Name the blood parasite species.
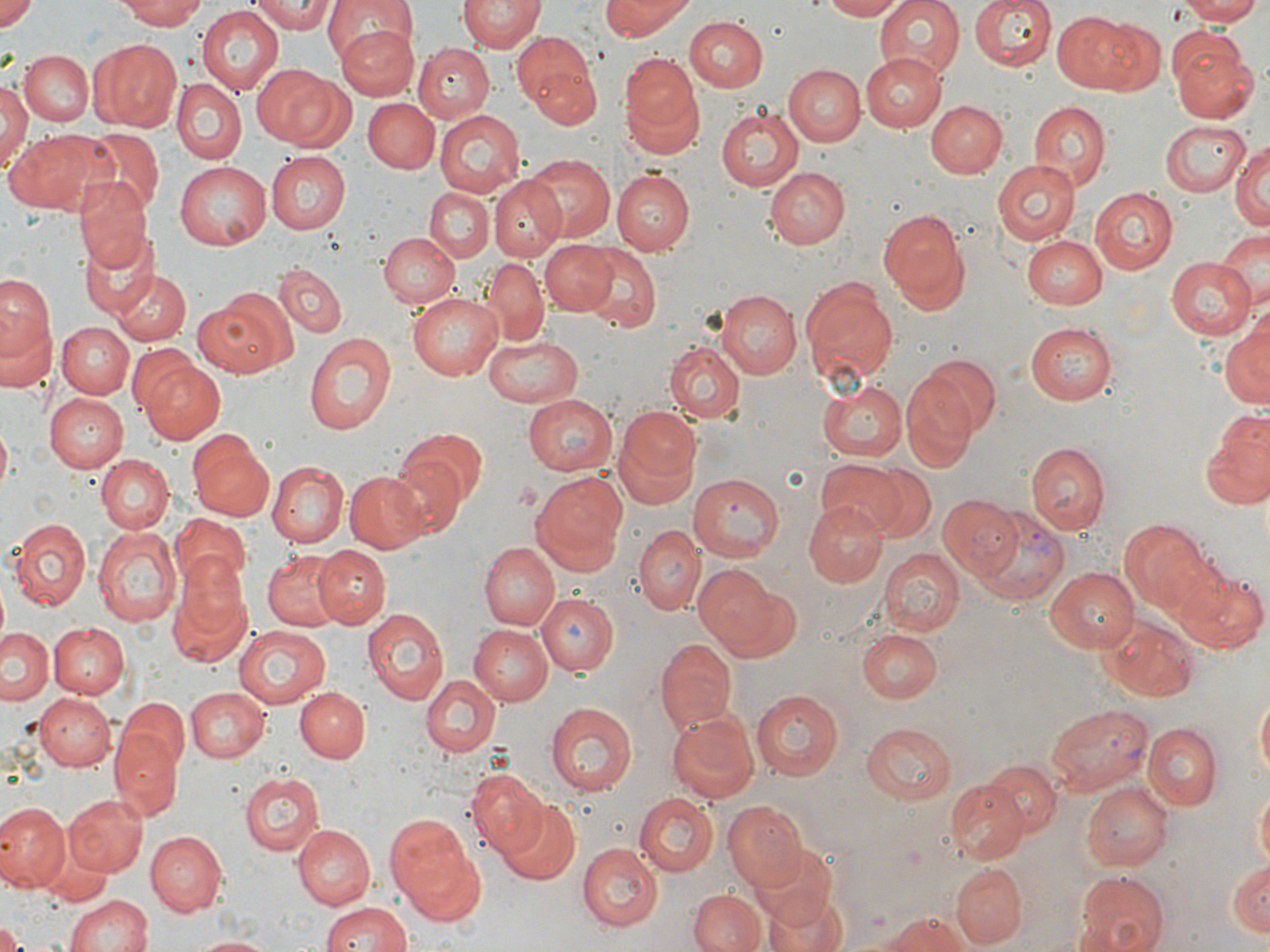
Plasmodium vivax.

Approximate bounding boxes as (x1,y1)-(x2,y2) corner pairs in pixels. Plasmodium vivax-infected red blood cell locations: (974,509)-(1069,603), (1046,703)-(1152,795). Uninfected red blood cell locations: (0,0)-(39,34), (123,0)-(208,26), (248,0)-(335,33), (321,0)-(413,68), (598,0)-(696,39), (818,0)-(910,21), (871,0)-(967,81), (968,0)-(1057,71), (1174,0)-(1264,25), (457,1)-(542,55), (196,5)-(283,96), (1055,10)-(1156,94), (694,11)-(774,158), (684,17)-(766,93), (334,25)-(417,97), (513,31)-(602,129), (1168,33)-(1256,121), (91,39)-(182,132), (412,44)-(494,123), (19,49)-(93,126), (619,53)-(703,151), (862,53)-(946,132), (253,62)-(343,149), (784,64)-(865,145), (172,80)-(246,164), (0,85)-(30,173), (363,99)-(441,174), (929,101)-(1006,177), (1027,102)-(1110,192), (716,106)-(804,193), (436,111)-(525,195), (1157,119)-(1248,198), (77,128)-(164,214), (1191,128)-(1270,211), (6,129)-(111,216), (1231,141)-(1270,233), (266,151)-(351,233), (524,154)-(613,243), (993,160)-(1081,244), (175,162)-(271,249), (765,168)-(849,250), (615,170)-(694,254), (488,176)-(567,260), (74,179)-(155,276), (425,187)-(494,261), (1089,188)-(1177,275), (400,207)-(489,304), (879,207)-(972,312), (1216,228)-(1270,314), (378,231)-(459,306), (78,235)-(163,320), (1025,236)-(1106,309), (539,240)-(620,314), (579,246)-(665,334), (481,257)-(549,342), (1165,257)-(1257,339), (275,264)-(346,337), (111,267)-(191,346), (0,271)-(54,361), (798,274)-(898,392), (195,289)-(295,378), (716,290)-(801,378), (407,292)-(505,380), (2,311)-(58,394), (1221,311)-(1269,411), (1025,319)-(1118,403), (58,321)-(134,398), (304,333)-(397,433), (483,333)-(585,405), (664,342)-(744,420), (919,354)-(1004,435), (139,360)-(227,444), (901,373)-(981,470), (816,379)-(907,461), (520,393)-(617,477), (44,394)-(128,472), (614,406)-(702,501), (1204,407)-(1270,512), (393,427)-(485,526), (188,431)-(275,521), (1028,442)-(1110,534), (96,454)-(173,532), (815,460)-(910,539), (267,461)-(349,546), (381,461)-(458,539), (345,470)-(430,553), (532,471)-(629,568), (689,474)-(783,559), (936,496)-(1023,579), (805,502)-(887,586), (169,516)-(252,590), (11,518)-(91,609), (1120,521)-(1215,614), (93,525)-(183,629), (635,526)-(704,614), (481,542)-(558,629), (314,545)-(390,627), (879,549)-(963,637), (263,550)-(347,629), (167,561)-(253,667), (693,565)-(797,661), (1045,567)-(1142,653), (1172,567)-(1267,653), (536,594)-(619,675), (362,610)-(448,705), (1100,616)-(1201,703), (46,621)-(129,700), (470,624)-(553,704), (235,627)-(331,708), (2,628)-(55,707), (856,630)-(939,702), (655,640)-(736,733), (422,676)-(500,757), (185,686)-(271,761), (295,687)-(368,761), (751,688)-(846,779), (1254,693)-(1269,787), (35,696)-(115,772), (114,696)-(190,782), (547,703)-(639,797), (665,710)-(761,803), (863,722)-(957,803), (1143,723)-(1220,809), (111,730)-(182,817), (984,760)-(1058,835), (240,772)-(324,857), (469,777)-(552,861), (948,782)-(1028,864), (1084,783)-(1174,872), (1252,783)-(1269,876), (63,794)-(147,877), (634,794)-(718,877), (492,800)-(581,885), (723,803)-(810,893), (0,805)-(68,893), (384,811)-(485,920), (296,823)-(376,907), (40,832)-(111,906), (146,832)-(226,916), (578,845)-(663,931), (757,854)-(838,930), (1226,858)-(1269,941), (952,864)-(1026,945), (1073,871)-(1170,952), (762,883)-(849,952), (689,890)-(764,952), (64,893)-(154,951), (319,900)-(414,952), (885,913)-(976,952), (1,924)-(25,952), (189,934)-(280,952). 1000x magnification. Optical microscopy. Single field of view. May-Grünwald-Giemsa-stained preparation. Thin blood film. Image is 1270×952 pixels.